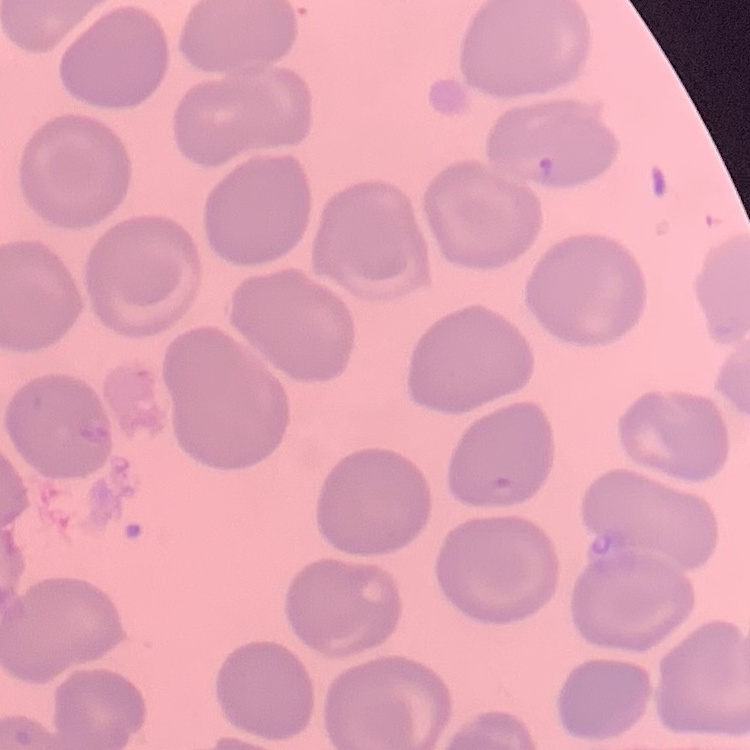 The erythrocytes show no rouleaux formation. Square crop of a larger photomicrograph. Stained with either Field's or Giemsa. Thin blood smear.